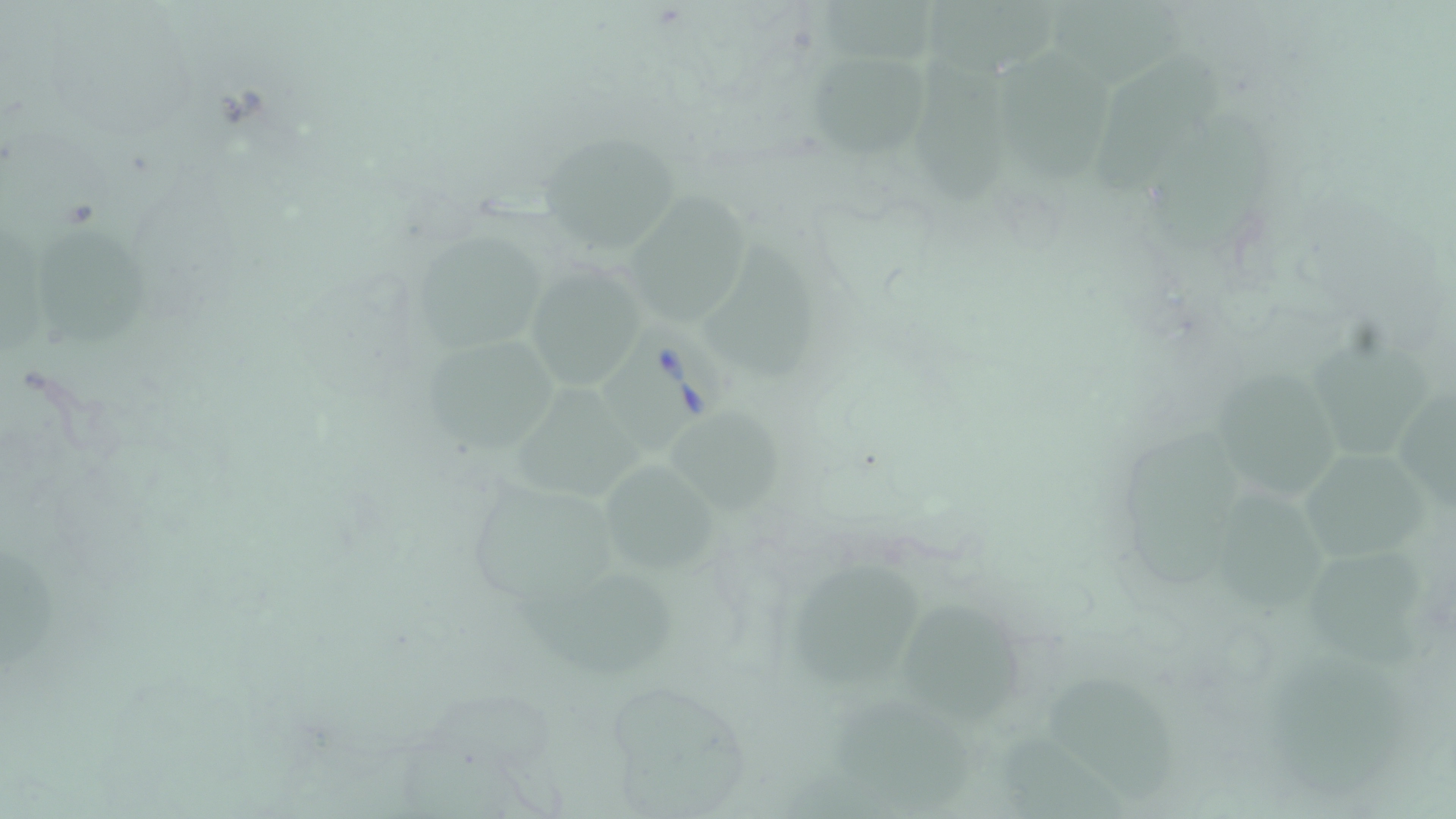 Approximate bounding boxes as [x1, y1, x2, y2] in pixels. Babesia divergens-infected red blood cell locations: [601, 320, 730, 458]. Uninfected red blood cell locations: [822, 0, 950, 63], [927, 0, 1067, 76], [1050, 1, 1185, 85], [998, 48, 1113, 184], [1098, 49, 1221, 192], [805, 51, 929, 162], [919, 51, 1018, 207], [1153, 113, 1269, 248], [538, 132, 682, 256], [627, 193, 753, 327], [36, 228, 149, 351], [417, 231, 545, 353], [706, 242, 818, 382], [522, 263, 651, 393], [1306, 330, 1427, 462], [425, 336, 560, 452], [1212, 365, 1341, 499], [1399, 382, 1456, 512], [513, 384, 644, 499], [669, 413, 784, 517], [1118, 427, 1237, 586], [1295, 448, 1441, 568], [603, 463, 720, 575], [1211, 488, 1326, 608], [1310, 535, 1418, 669], [0, 547, 56, 670], [511, 569, 677, 677], [792, 569, 921, 687], [899, 599, 1024, 725], [1267, 653, 1402, 792], [1043, 675, 1176, 804], [837, 701, 972, 809]. Slide-level diagnosis: Babesia divergens. Light microscopy. One field of a larger specimen. Image is 1456×819 pixels. May-Grünwald-Giemsa stain. Thin blood film. 1000x magnification.